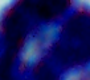
Summary:
  - Identification: leukocyte
  - Modality: photomicrograph
  - Magnification: 1000x